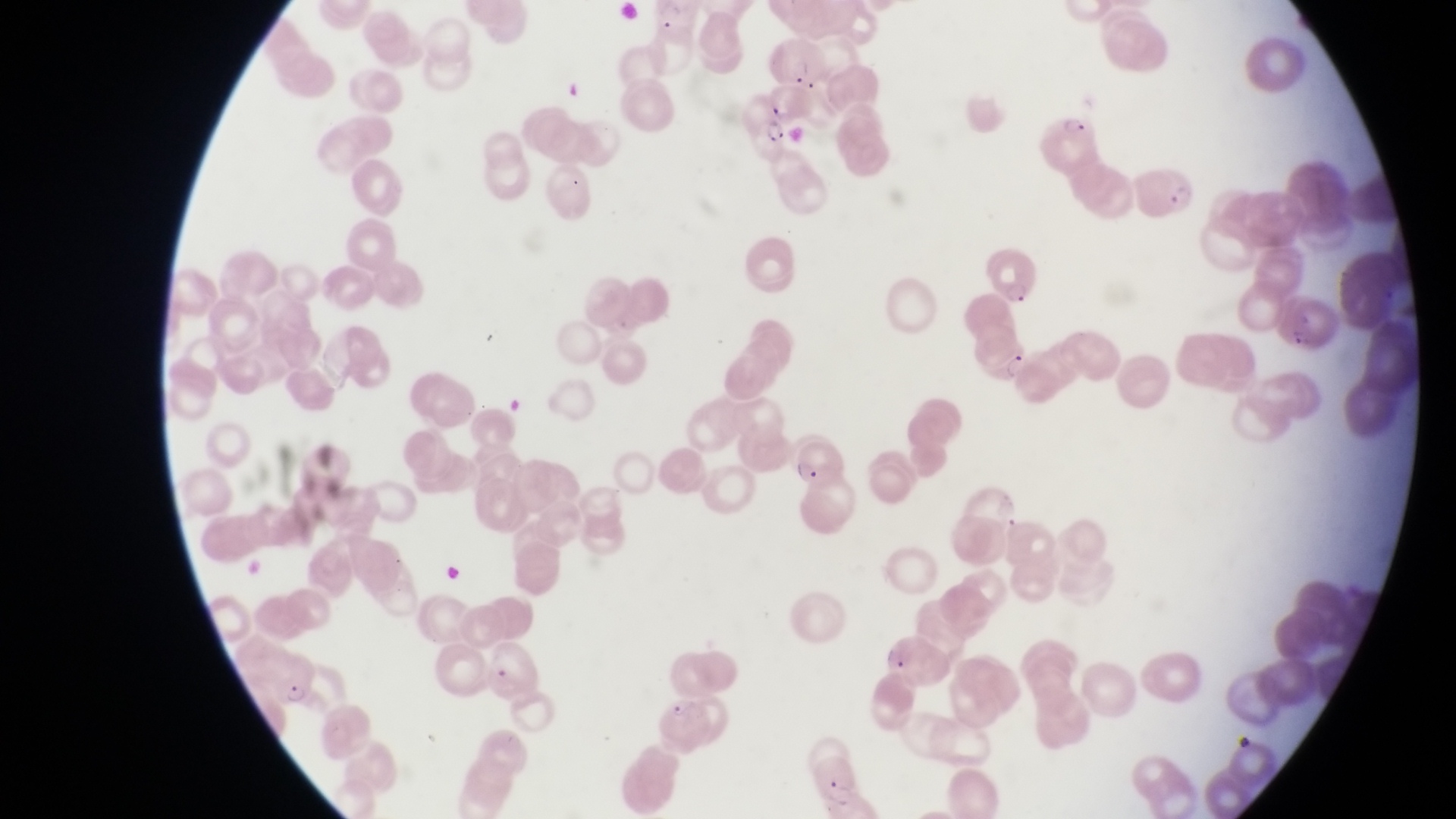
Approximate bounding boxes as left top right bottom in pixels.
Summary:
  - Parasitised red blood cell locations: 732 87 798 158; 1049 105 1098 174; 1136 158 1195 217; 993 248 1045 304; 1285 290 1340 356; 975 322 1030 386; 793 430 845 490; 262 657 323 707; 657 693 716 752; 814 753 863 808
  - Magnification: 1000x
  - Field of view: single
  - Capture: smartphone photograph through the eyepiece of an Olympus CX-23 microscope
  - Preparation: thin blood smear
  - Country: Uganda
  - Image size: 1456×819 pixels